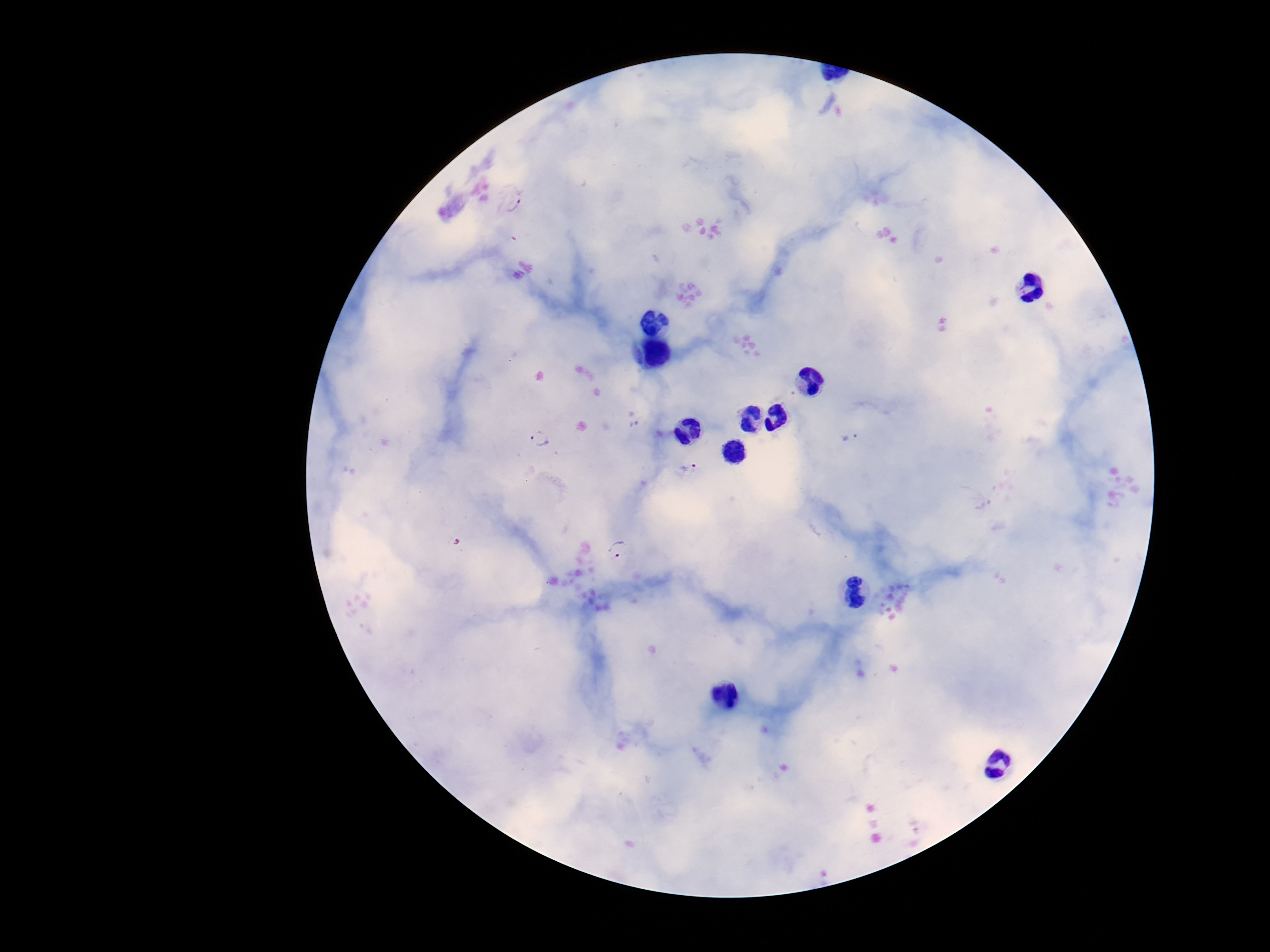
Approximate object centers, in pixels from the top-left corner. Plasmodium parasite locations: (x=509, y=201), (x=851, y=437), (x=539, y=438), (x=687, y=468), (x=619, y=549). Single field of view. Thick blood film. Smartphone photograph taken through the microscope eyepiece. Giemsa-stained preparation. Patient malaria status: positive. Image is 1270×952 pixels. 100x magnification.